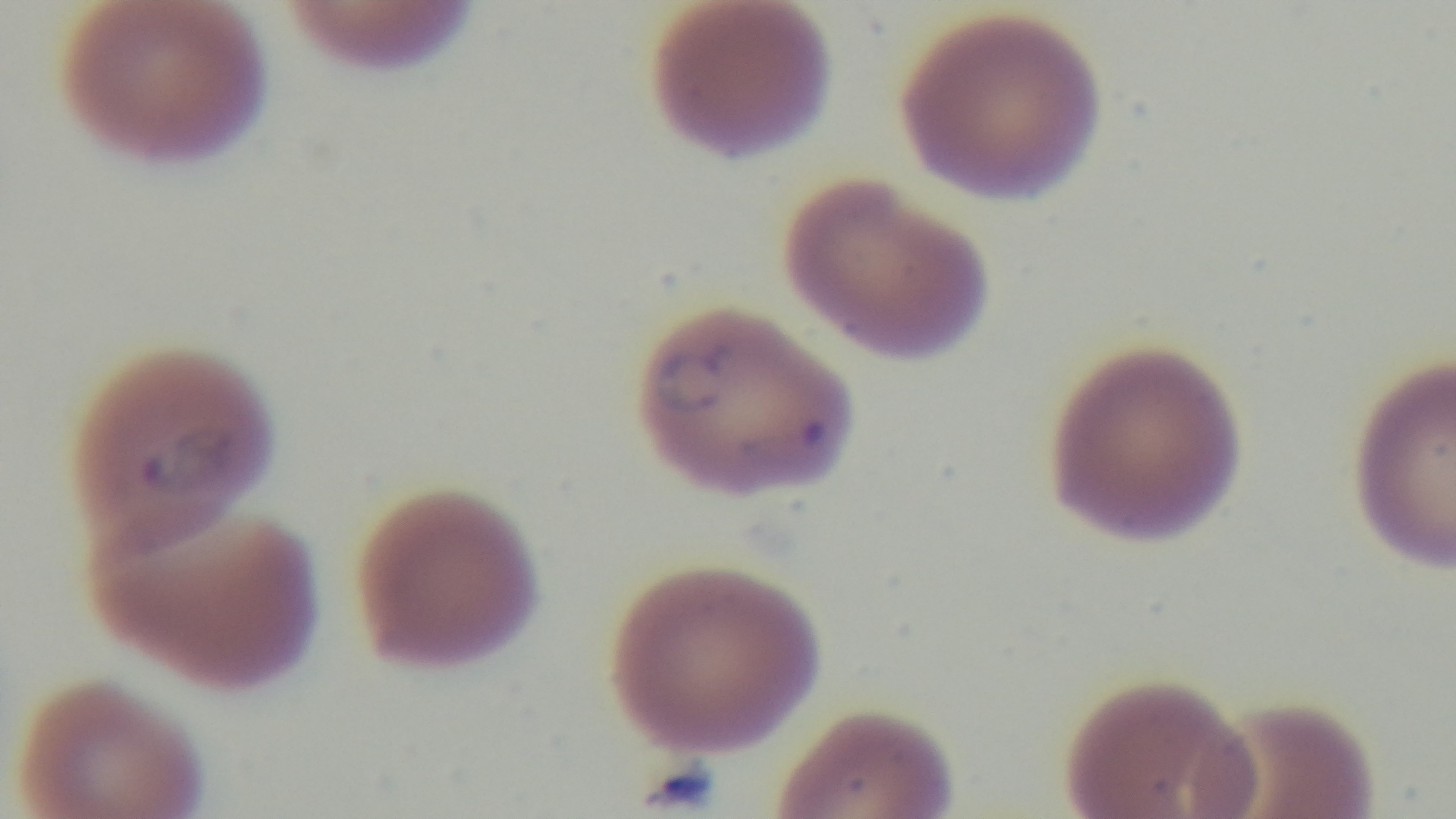
{
  "capture": "mounted 4K digital camera",
  "preparation": "thin",
  "malaria_status": "infected",
  "modality": "light microscopy",
  "stain": "Giemsa",
  "objective": "100x oil immersion",
  "field_of_view": "one from the slide"
}